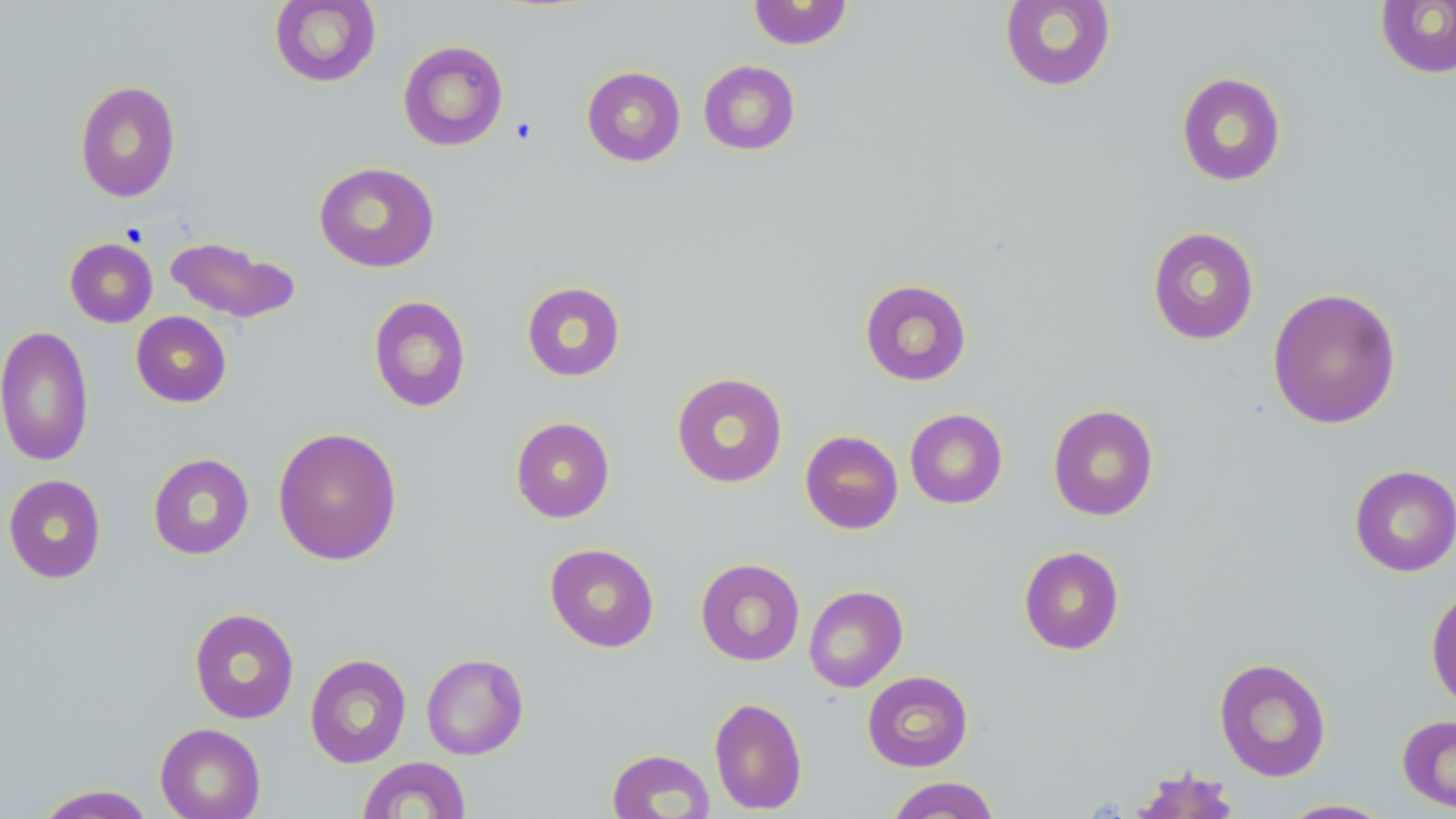

Summary:
  - Coordinate format: approximate bounding boxes as named x1/y1/x2/y2 corners in pixels
  - Platelet locations: (x1=510, y1=117, x2=538, y2=144)
  - Uninfected red blood cell locations: (x1=270, y1=0, x2=381, y2=88), (x1=748, y1=0, x2=853, y2=50), (x1=1376, y1=0, x2=1456, y2=78), (x1=999, y1=1, x2=1116, y2=92), (x1=397, y1=39, x2=509, y2=151), (x1=698, y1=60, x2=800, y2=156), (x1=581, y1=66, x2=685, y2=166), (x1=1176, y1=72, x2=1287, y2=187), (x1=74, y1=80, x2=181, y2=203), (x1=314, y1=161, x2=439, y2=272), (x1=1147, y1=226, x2=1259, y2=345), (x1=164, y1=235, x2=300, y2=324), (x1=65, y1=238, x2=158, y2=327), (x1=859, y1=278, x2=972, y2=386), (x1=521, y1=281, x2=626, y2=381), (x1=1266, y1=287, x2=1402, y2=429), (x1=368, y1=295, x2=472, y2=413), (x1=131, y1=311, x2=232, y2=407), (x1=0, y1=325, x2=95, y2=466), (x1=671, y1=372, x2=788, y2=488), (x1=1047, y1=404, x2=1159, y2=521), (x1=905, y1=408, x2=1008, y2=509), (x1=510, y1=416, x2=615, y2=523), (x1=273, y1=427, x2=402, y2=565), (x1=800, y1=430, x2=903, y2=534), (x1=148, y1=453, x2=254, y2=560), (x1=1349, y1=464, x2=1456, y2=577), (x1=3, y1=474, x2=106, y2=583), (x1=545, y1=543, x2=659, y2=652), (x1=1018, y1=546, x2=1125, y2=655), (x1=695, y1=558, x2=805, y2=666), (x1=1426, y1=584, x2=1456, y2=711), (x1=803, y1=585, x2=907, y2=692), (x1=188, y1=608, x2=300, y2=724), (x1=305, y1=653, x2=411, y2=768), (x1=421, y1=653, x2=528, y2=760), (x1=1214, y1=657, x2=1332, y2=781), (x1=862, y1=670, x2=973, y2=772), (x1=709, y1=696, x2=807, y2=814), (x1=1397, y1=714, x2=1456, y2=814), (x1=154, y1=723, x2=266, y2=819), (x1=607, y1=748, x2=715, y2=818), (x1=358, y1=756, x2=472, y2=818), (x1=1130, y1=766, x2=1242, y2=818), (x1=885, y1=776, x2=1001, y2=819), (x1=34, y1=784, x2=155, y2=818), (x1=1279, y1=798, x2=1392, y2=818)
  - Slide-level diagnosis: negative for blood parasites
  - Preparation: thin blood film
  - Image size: 1456×819 pixels
  - Magnification: 1000x
  - Modality: light microscopy
  - Field of view: one of a larger specimen
  - Stain: May-Grünwald-Giemsa